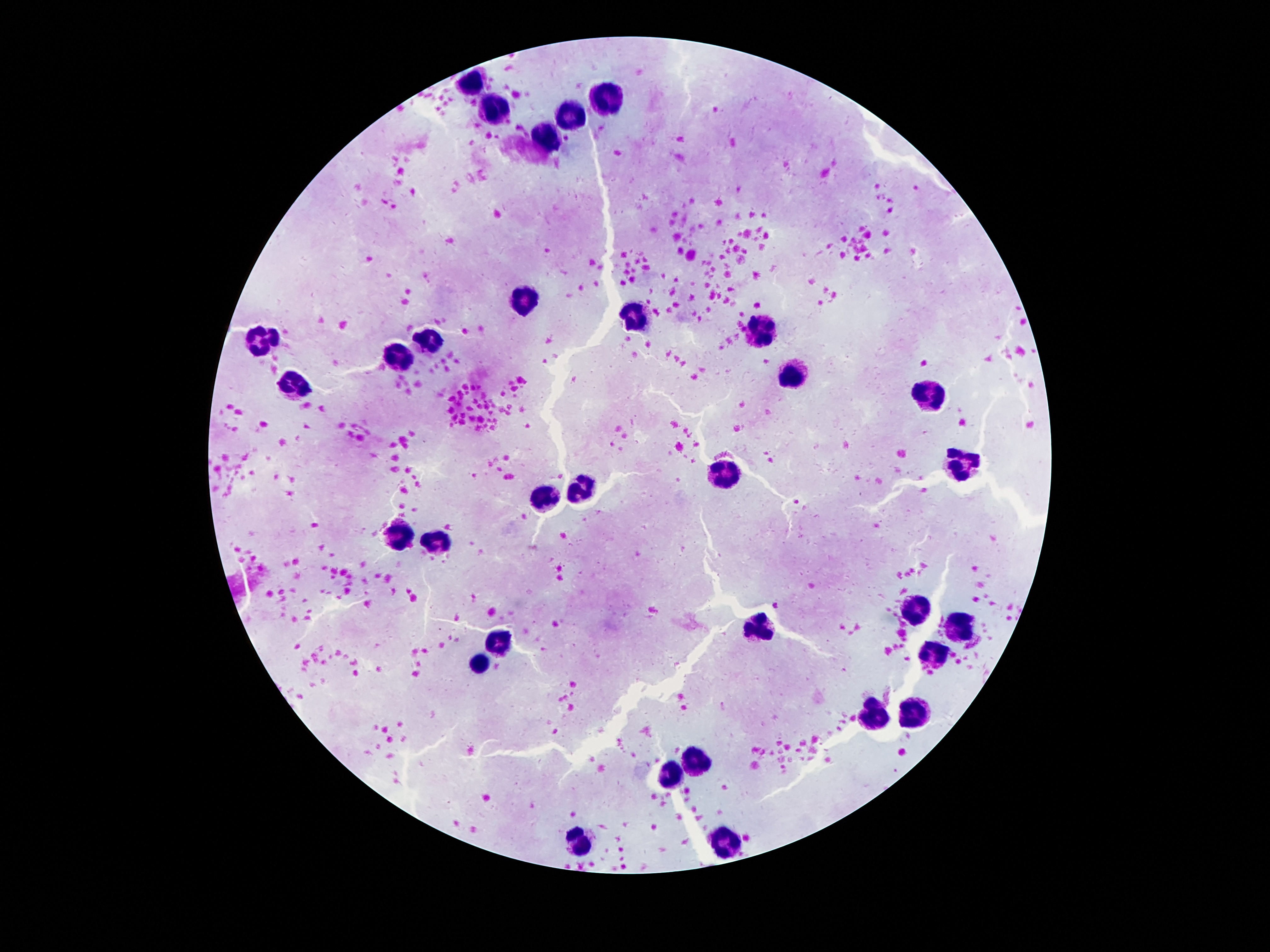
Approximate centers as (x, y) in pixels.
Summary:
  - Leukocyte locations: (470, 85), (606, 99), (569, 113), (502, 116), (552, 137), (529, 298), (641, 321), (757, 329), (435, 338), (262, 339), (403, 357), (791, 375), (293, 381), (929, 390), (969, 464), (729, 471), (579, 488), (546, 497), (399, 536), (436, 544), (917, 612), (764, 626), (959, 629), (504, 639), (934, 654), (480, 661), (875, 711), (915, 715), (700, 761), (666, 774), (576, 841), (725, 842)
  - Image size: 1270×952 pixels
  - Preparation: thick blood film
  - Patient malaria status: negative
  - Stain: Giemsa
  - Field of view: single
  - Capture: smartphone camera through the microscope eyepiece
  - Magnification: 100x